State which cell type is depicted.
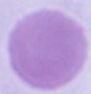
An erythrocyte.

Captured at 1000x magnification. Photomicrograph.